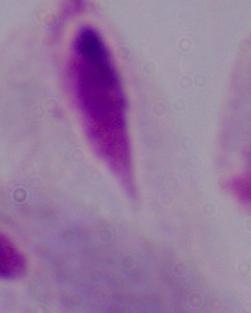

magnification = 1000x
identification = trichomonad
modality = photomicrograph